Comment on the morphology of the erythrocytes.
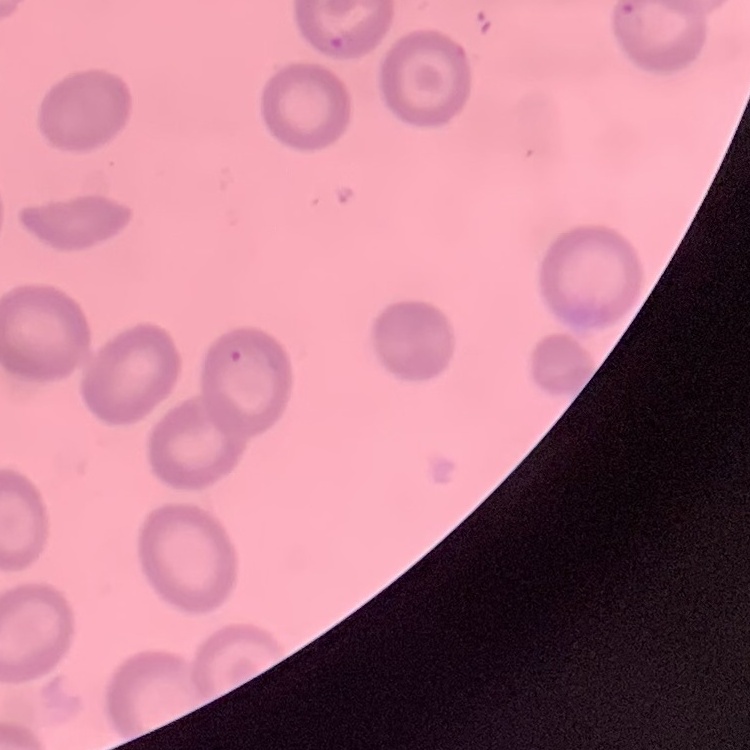
They show no rouleaux formation.

Thin blood smear. Square crop of a larger photomicrograph. Stained with either Field's or Giemsa.